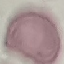

Summary:
  - Result: negative for malaria parasites
  - Capture: smartphone camera at the microscope eyepiece
  - Stain: Giemsa
  - Preparation: thin smear
  - Image type: cell patch, automatically extracted from a larger field of view and resized to 64 × 64 pixels